Report the malaria status of this cell.
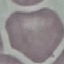
Uninfected.

image type = cell patch, automatically extracted from a larger field of view and resized to 64 × 64 pixels
capture = smartphone camera at the microscope eyepiece
preparation = thin blood film
stain = Giemsa